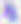 Micrograph. Toxoplasma gondii is shown. 400x magnification.